Name the parasite shown.
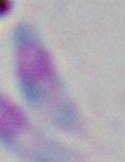

This is Toxoplasma gondii.

Summary:
  - Magnification: 1000x
  - Modality: photomicrograph